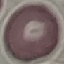

Malaria status: uninfected. Acquired by smartphone through the microscope eyepiece. Thin blood film. Giemsa-stained preparation. Automatically extracted cell patch, resized to 64 × 64 pixels.